Locate and identify every blood parasite.
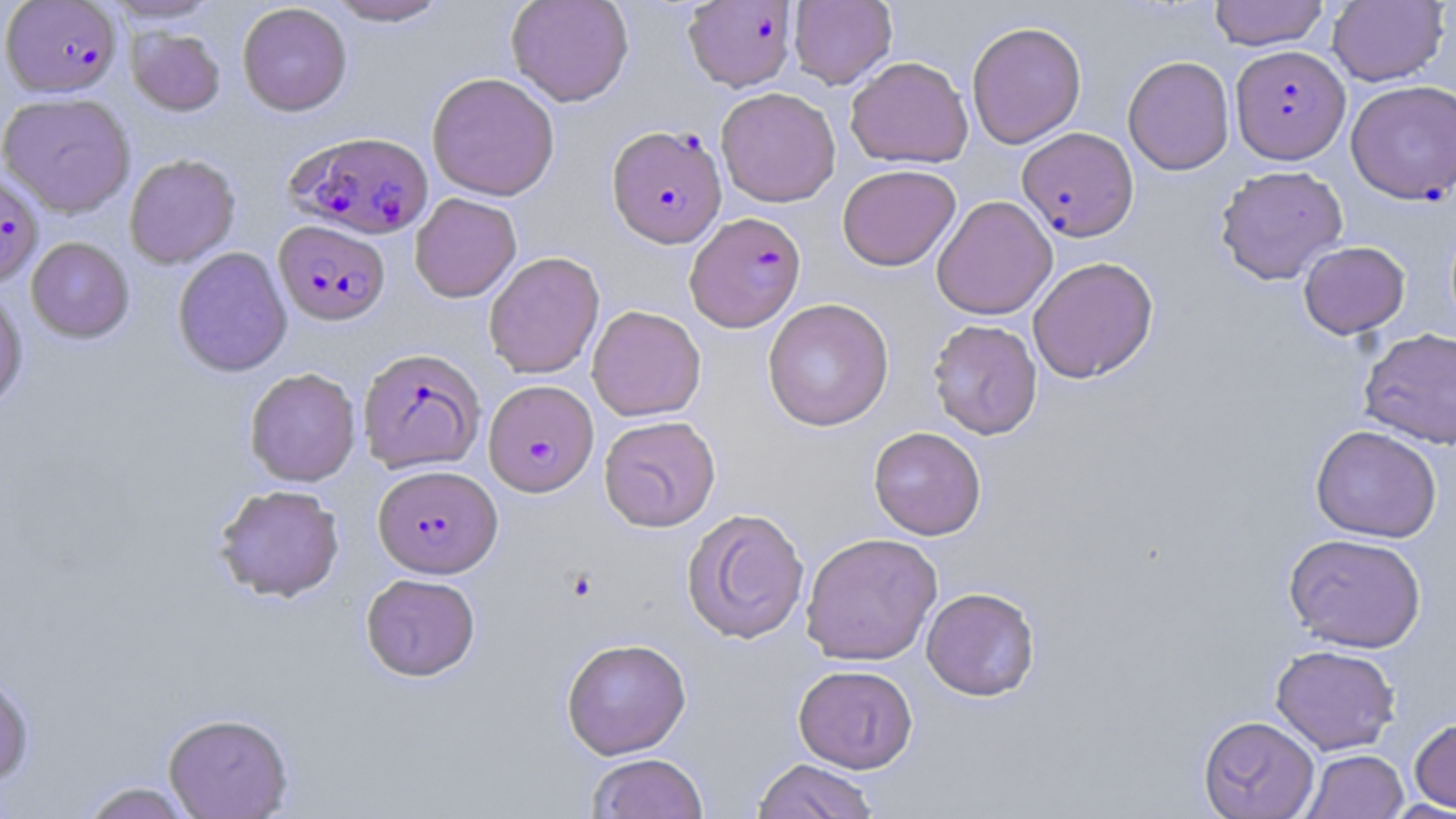

Approximate bounding boxes as [x1, y1, x2, y2] in pixels.
Plasmodium falciparum-infected red blood cells: [2, 1, 122, 97], [682, 1, 798, 92], [1230, 44, 1349, 164], [1345, 79, 1456, 204], [607, 124, 727, 248], [1017, 127, 1139, 242], [289, 130, 434, 239], [0, 172, 43, 287], [685, 211, 807, 332], [274, 220, 391, 326], [357, 347, 485, 473], [483, 379, 599, 497], [373, 464, 503, 578].
No Plasmodium ovale, Plasmodium malariae, Plasmodium vivax, Babesia divergens, or Trypanosoma brucei observed.

slide-level diagnosis = Plasmodium falciparum
preparation = thin blood film
image size = 1456×819 pixels
stain = May-Grünwald-Giemsa
modality = light microscopy
magnification = 1000x
field of view = single
uninfected red blood cell locations = approximate bounding boxes as [x1, y1, x2, y2] in pixels: [101, 0, 225, 24], [325, 0, 451, 26], [505, 0, 634, 107], [788, 0, 897, 89], [1209, 0, 1329, 50], [1327, 1, 1449, 86], [237, 3, 352, 116], [966, 20, 1087, 149], [127, 27, 225, 115], [845, 56, 973, 169], [1122, 56, 1235, 175], [427, 72, 560, 201], [716, 87, 841, 207], [0, 92, 136, 217], [124, 153, 241, 268], [837, 164, 961, 271], [1215, 165, 1348, 285], [410, 193, 521, 302], [931, 195, 1057, 320], [26, 237, 134, 342], [1298, 240, 1410, 339], [172, 247, 293, 378], [483, 252, 605, 379], [1028, 256, 1158, 383], [0, 287, 28, 413], [762, 298, 894, 431], [587, 305, 706, 421], [928, 318, 1043, 439], [1358, 328, 1456, 448], [244, 368, 361, 486], [599, 415, 721, 532], [1310, 425, 1442, 542], [868, 426, 987, 540], [214, 484, 345, 602], [681, 507, 810, 644], [800, 532, 943, 666], [1284, 532, 1427, 652], [361, 573, 481, 681], [921, 586, 1040, 701], [561, 638, 691, 759], [1270, 644, 1400, 754], [793, 664, 918, 773], [0, 670, 35, 788], [163, 712, 294, 818], [1198, 715, 1320, 818], [1409, 716, 1456, 813], [1301, 749, 1408, 818], [587, 752, 709, 818], [753, 758, 879, 818], [77, 781, 198, 819]